Assess this cell for malaria.
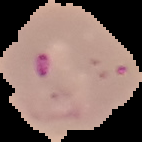
Parasitized.

preparation: thin blood smear
image_size: 142×142 pixels
image_type: segmented cell region with the area outside set to black